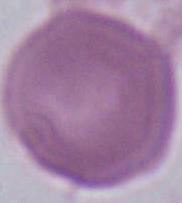
{
  "magnification": "1000x",
  "modality": "photomicrograph",
  "identification": "erythrocyte"
}